Assess this cell for malaria.
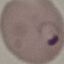

Parasitized.

Summary:
  - Image type: automatically extracted cell patch, resized to 64 × 64 pixels
  - Capture: smartphone camera at the microscope eyepiece
  - Stain: Giemsa
  - Preparation: thin blood film